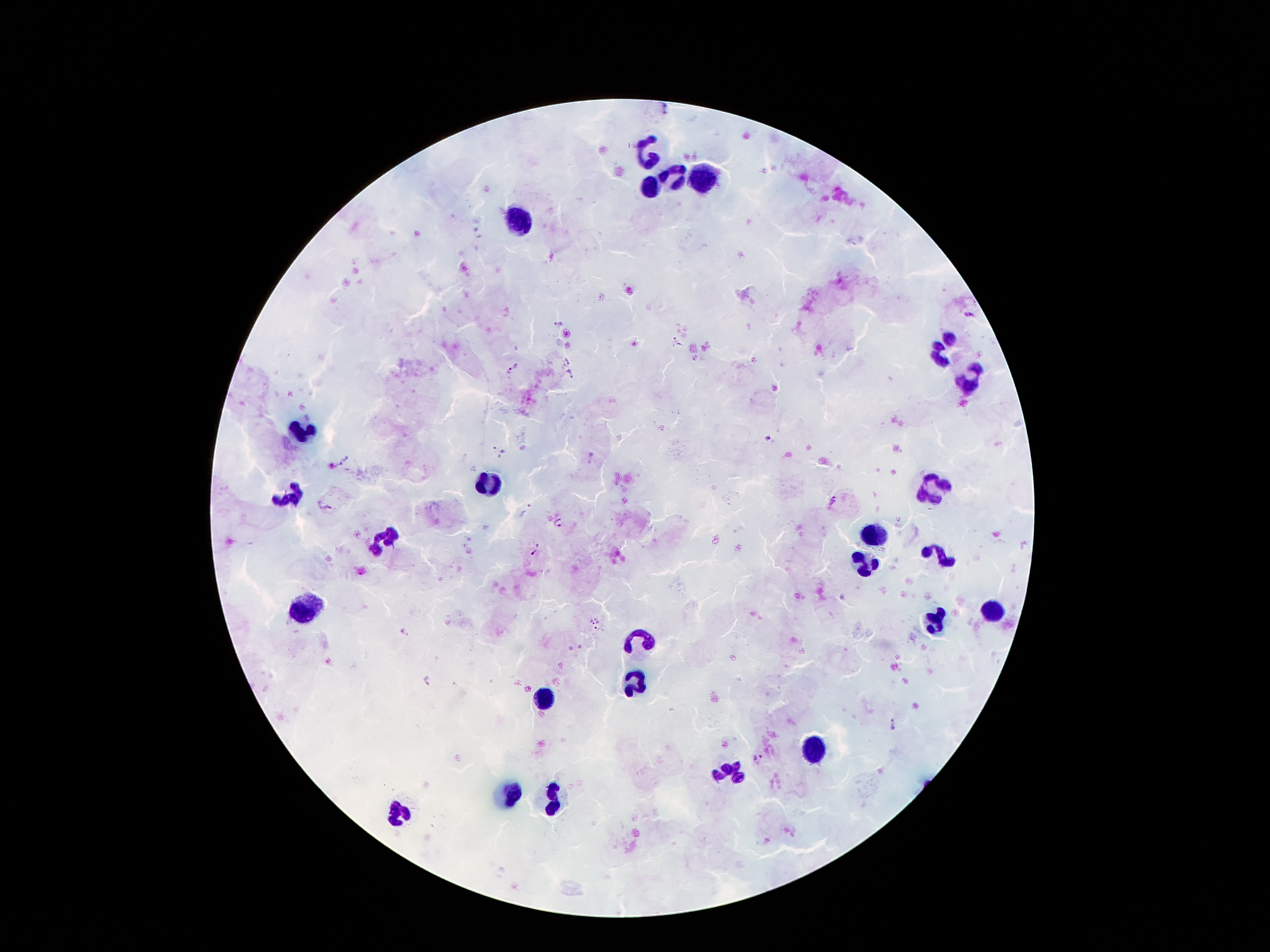
magnification: 100x
plasmodium_parasite_locations: 'approximate centers as {x, y} in pixels: {666, 109}, {968, 316}, {558, 323}, {677, 342}, {567, 362}, {517, 365}, {508, 371}, {571, 374}, {767, 439}, {498, 449}, {592, 459}, {345, 460}, {832, 501}, {327, 507}, {527, 511}, {560, 522}, {537, 549}, {597, 624}, {405, 632}, {428, 681}, {895, 725}, {759, 759}'
capture: smartphone through the microscope eyepiece
leukocyte_locations: 'approximate centers as {x, y} in pixels: {645, 151}, {673, 176}, {704, 176}, {652, 187}, {524, 218}, {942, 346}, {969, 382}, {301, 432}, {490, 483}, {931, 489}, {286, 495}, {879, 529}, {385, 537}, {942, 552}, {862, 563}, {992, 611}, {305, 613}, {931, 623}, {637, 638}, {635, 684}, {543, 697}, {811, 747}, {732, 772}, {511, 796}, {553, 804}, {400, 814}'
field_of_view: one from this slide
patient_malaria_status: positive for Plasmodium falciparum
preparation: thick blood film
image_size: 1270×952 pixels
stain: Giemsa